Name the blood parasite species.
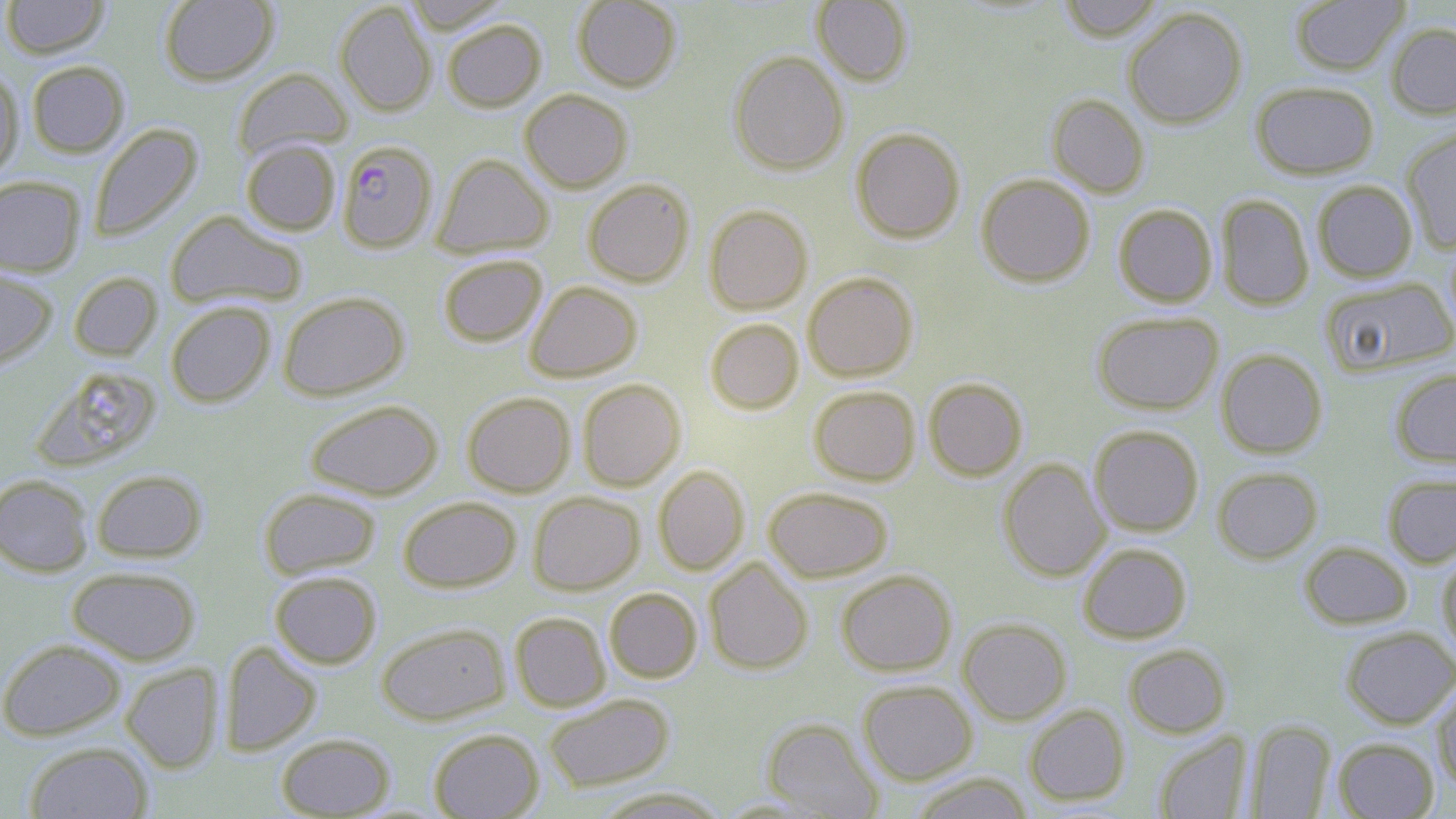
Plasmodium falciparum.

Approximate bounding boxes as (x1,y1)-(x2,y2) corner pairs in pixels. Uninfected red blood cell locations: (1,0)-(110,58), (159,0)-(278,86), (404,0)-(511,33), (572,0)-(681,92), (1057,0)-(1164,42), (1290,0)-(1409,75), (811,1)-(913,87), (335,2)-(436,116), (1123,7)-(1247,129), (442,18)-(546,112), (1386,23)-(1456,119), (728,50)-(849,175), (26,60)-(129,157), (0,66)-(24,181), (232,68)-(353,160), (1250,81)-(1379,179), (519,89)-(632,192), (1047,94)-(1149,198), (89,123)-(203,242), (851,127)-(965,244), (1401,127)-(1456,253), (241,139)-(340,235), (433,153)-(554,258), (976,173)-(1095,287), (0,176)-(85,276), (583,178)-(695,287), (1312,180)-(1418,283), (1216,194)-(1314,311), (704,204)-(813,315), (1113,204)-(1218,308), (165,210)-(307,310), (437,254)-(548,347), (0,266)-(57,371), (68,272)-(163,361), (802,272)-(918,382), (1321,277)-(1456,377), (525,281)-(642,382), (277,291)-(409,400), (165,301)-(276,407), (1091,311)-(1223,415), (705,318)-(803,414), (1216,348)-(1327,459), (30,365)-(163,471), (1390,367)-(1456,469), (923,377)-(1028,481), (577,379)-(686,491), (809,385)-(920,486), (462,391)-(575,497), (305,399)-(443,500), (1089,425)-(1203,537), (998,458)-(1110,581), (653,465)-(750,575), (1212,467)-(1323,564), (91,469)-(207,562), (1383,473)-(1456,568), (0,474)-(95,577), (763,486)-(893,582), (258,487)-(381,579), (528,491)-(644,595), (398,496)-(521,592), (1299,541)-(1412,629), (1078,543)-(1192,643), (1437,552)-(1456,658), (704,558)-(813,674), (66,566)-(201,665), (837,569)-(957,676), (269,570)-(382,669), (604,587)-(702,683), (510,611)-(611,712), (958,617)-(1072,725), (375,622)-(510,725), (1341,626)-(1456,729), (0,638)-(126,740), (219,640)-(322,756), (1124,644)-(1230,738), (121,663)-(223,774), (857,680)-(978,784), (1431,680)-(1456,792), (543,693)-(674,792), (1024,704)-(1130,806), (762,718)-(883,818), (1245,720)-(1336,818), (428,728)-(544,819), (1154,732)-(1252,819), (276,733)-(395,817), (1333,737)-(1439,818), (24,741)-(153,819), (909,773)-(1034,819), (590,787)-(730,818). Plasmodium falciparum-infected red blood cell locations: (336,140)-(438,253). Thin blood film. Image is 1456×819 pixels. May-Grünwald-Giemsa-stained preparation. Single field of view. Light microscopy. Captured at 1000x magnification.